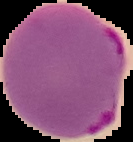
Image is 133×142 pixels. Segmented cell region on a black background. Result: Plasmodium parasites detected. From a thin blood smear.